Give the preparation type.
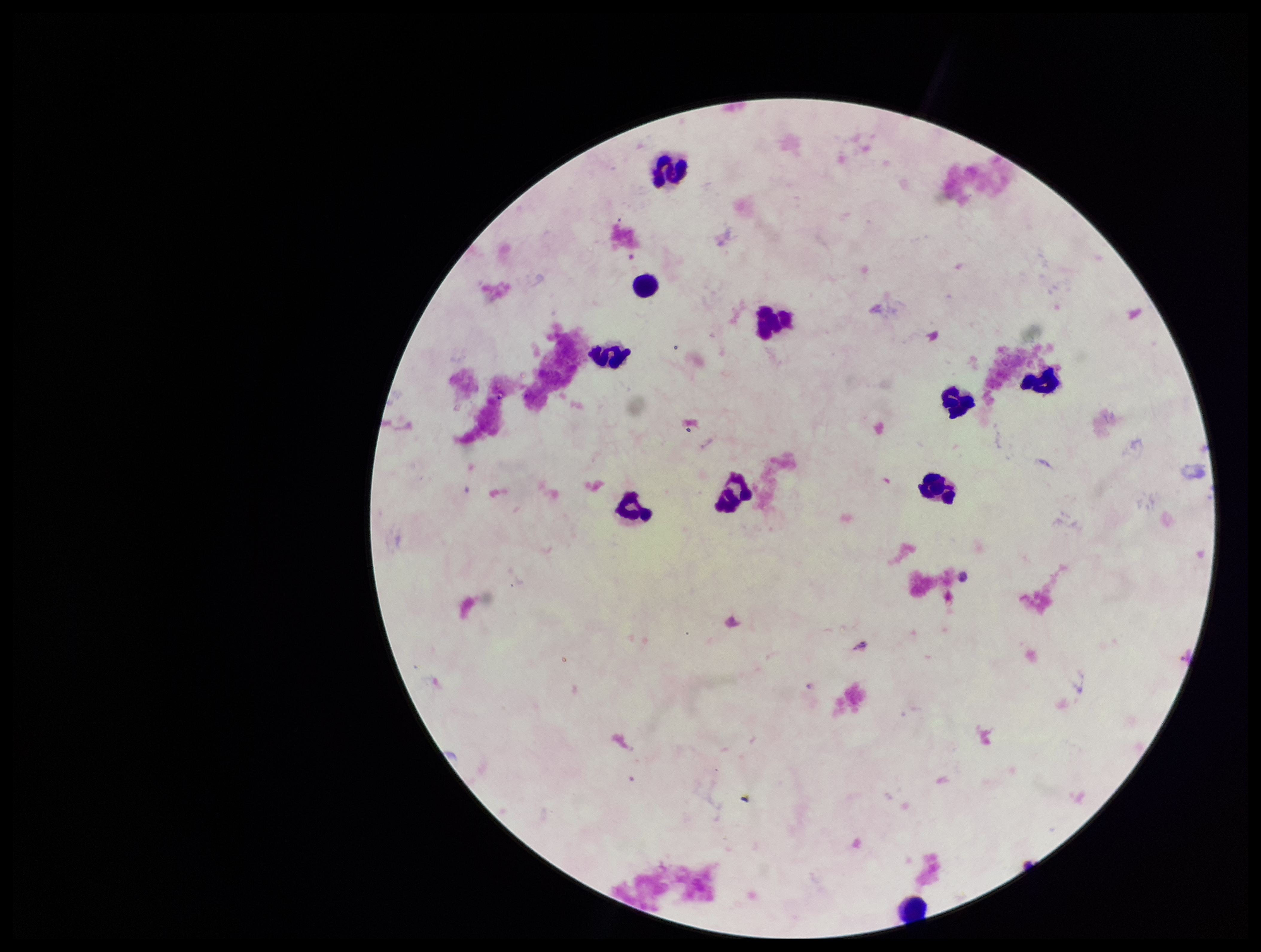

It is a thick blood smear.

Summary:
  - Stain: Giemsa
  - Image size: 1261×952 pixels
  - Leukocyte count: 10
  - Field of view: one from this slide
  - Plasmodium parasites: none identified
  - Patient malaria status: negative
  - Capture: smartphone photograph through the microscope eyepiece
  - Parasite count: 0